Classify this cell by malaria status.
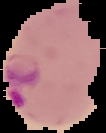
It is parasitized.

preparation = thin blood film
image size = 106×133 pixels
image type = segmented cell region with the area outside set to black